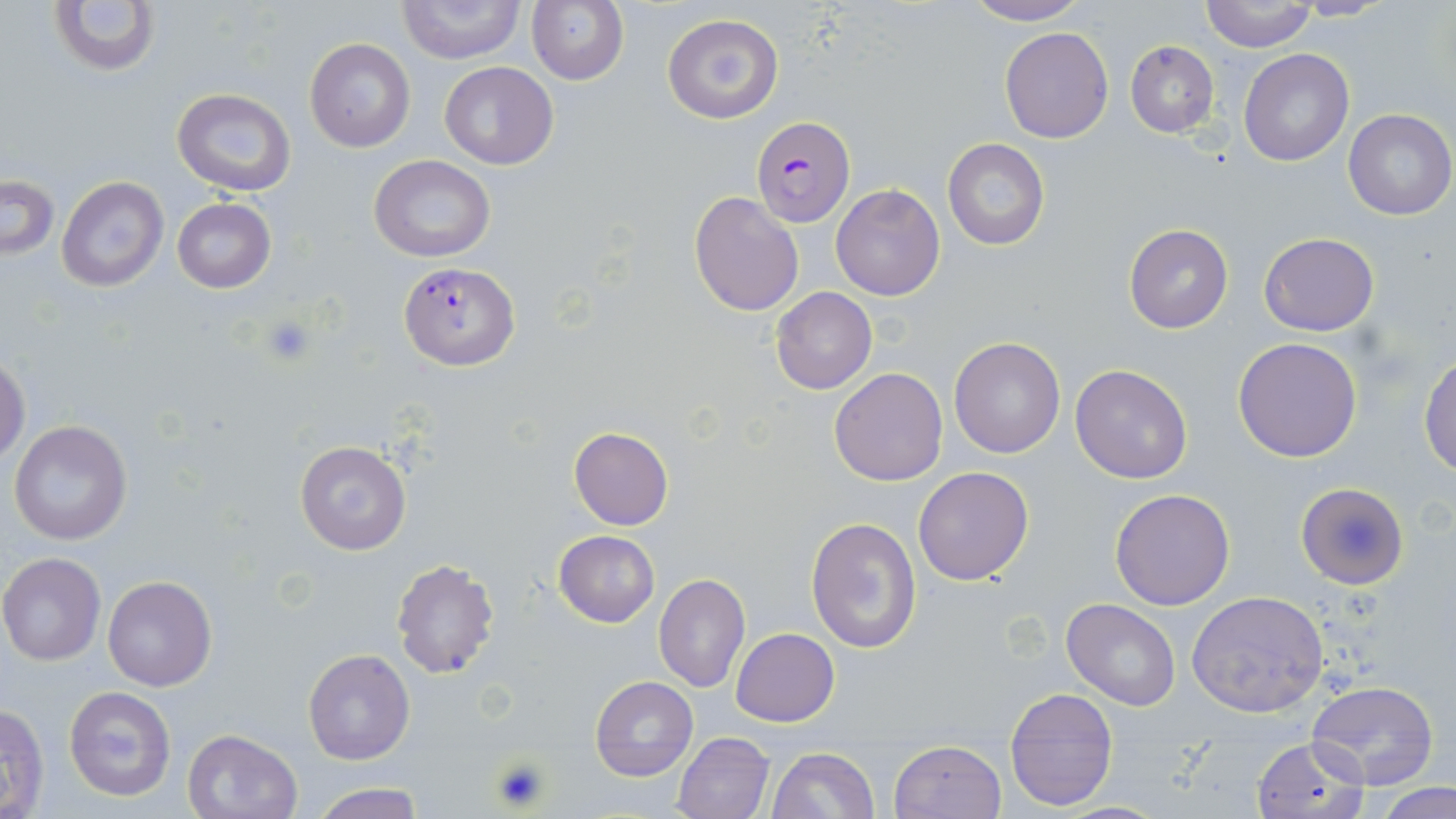
Approximate bounding boxes as (x1, y1, x2, y2) in pixels. Plasmodium falciparum-infected red blood cell locations: (752, 114, 855, 227), (397, 261, 519, 369). Platelet locations: (256, 312, 318, 367), (491, 756, 552, 812). Uninfected red blood cell locations: (50, 0, 159, 77), (963, 0, 1091, 26), (398, 1, 523, 63), (526, 1, 629, 85), (1199, 1, 1317, 52), (661, 13, 783, 125), (999, 26, 1113, 143), (305, 38, 414, 153), (1124, 40, 1219, 138), (1240, 49, 1354, 166), (440, 62, 559, 168), (172, 88, 296, 196), (1342, 109, 1454, 221), (942, 139, 1050, 251), (369, 154, 495, 261), (56, 175, 167, 291), (1, 176, 58, 261), (830, 184, 945, 301), (689, 190, 804, 317), (171, 198, 275, 293), (1124, 224, 1233, 333), (1259, 232, 1379, 335), (771, 286, 877, 395), (1233, 336, 1363, 462), (949, 337, 1066, 457), (1419, 352, 1456, 477), (0, 354, 29, 467), (1069, 363, 1193, 484), (829, 367, 948, 486), (8, 419, 133, 546), (569, 427, 674, 530), (294, 440, 412, 555), (913, 465, 1036, 586), (1294, 481, 1409, 590), (1110, 489, 1235, 610), (806, 516, 923, 656), (552, 529, 660, 627), (0, 552, 106, 665), (391, 558, 499, 679), (654, 574, 750, 693), (103, 575, 216, 691), (1187, 591, 1331, 719), (1062, 599, 1181, 710), (731, 628, 840, 727), (303, 648, 415, 764), (590, 675, 697, 781), (1304, 681, 1439, 790), (64, 686, 176, 801), (1004, 687, 1118, 812), (1, 702, 50, 818), (182, 728, 302, 819), (673, 730, 773, 819), (1250, 737, 1367, 818), (888, 739, 1005, 819), (767, 747, 879, 819), (1370, 782, 1456, 819), (305, 783, 429, 819). Slide-level diagnosis: Plasmodium falciparum. One field of a larger specimen. 1000x magnification. Thin blood smear. May-Grünwald-Giemsa stain. Image is 1456×819 pixels. Light microscopy.